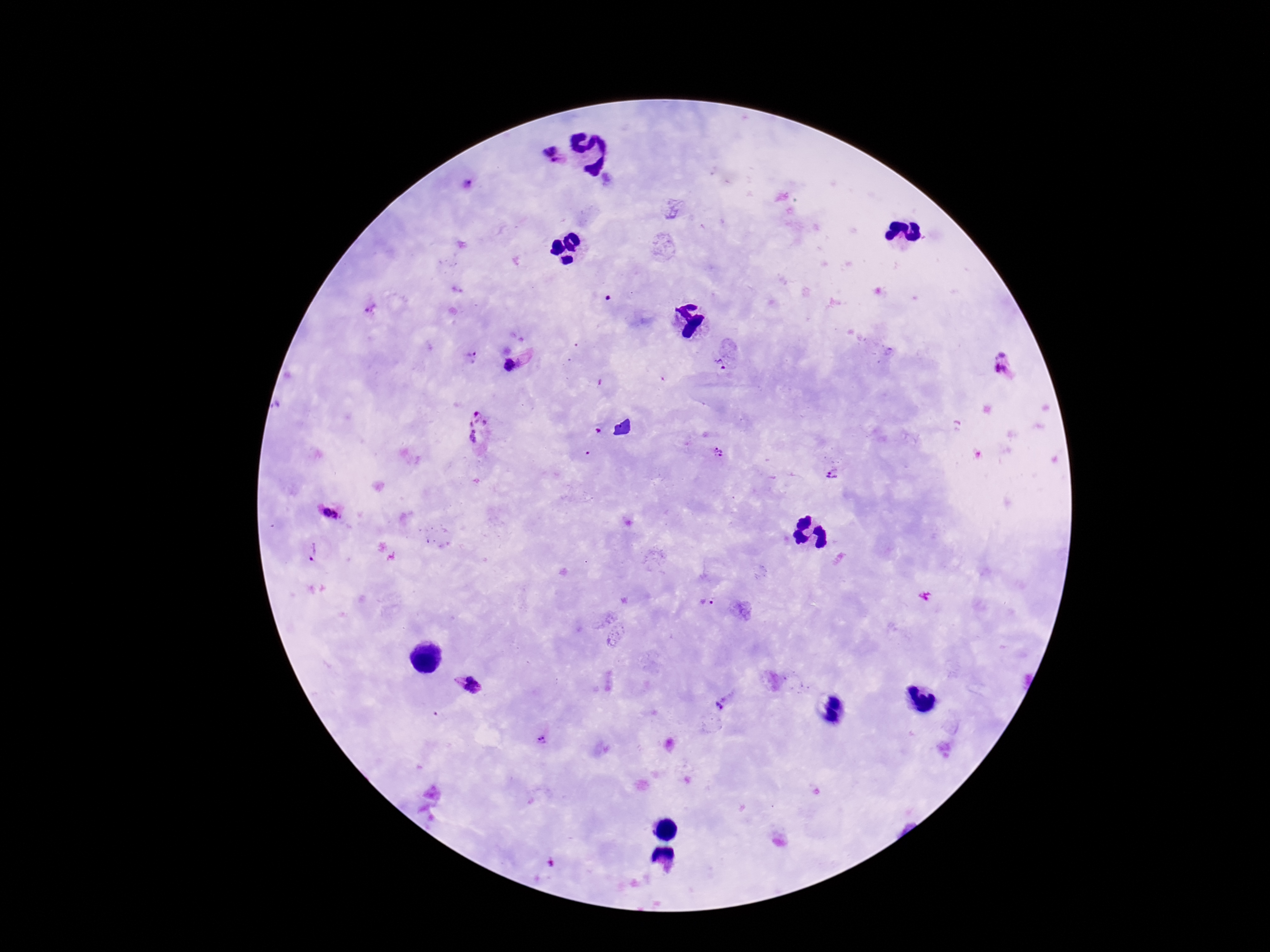

patient_malaria_status: infected
field_of_view: single
magnification: 100x
image_size: 1270×952 pixels
preparation: thick blood film
plasmodium_parasite_locations: 'approximate centers as [x, y] in pixels: [552, 155], [467, 183], [367, 309], [1002, 353], [472, 356], [719, 366], [510, 368], [1001, 369], [480, 432], [718, 453], [832, 475], [325, 513], [336, 516], [312, 551], [707, 603], [467, 685], [723, 705], [540, 740]'
capture: smartphone camera through the microscope eyepiece
stain: Giemsa